Report the malaria status of this cell.
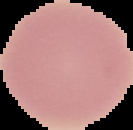

Uninfected.

Summary:
  - Image type: cell region segmented out of the field of view; surrounding area masked to black
  - Preparation: thin blood smear
  - Image size: 133×130 pixels